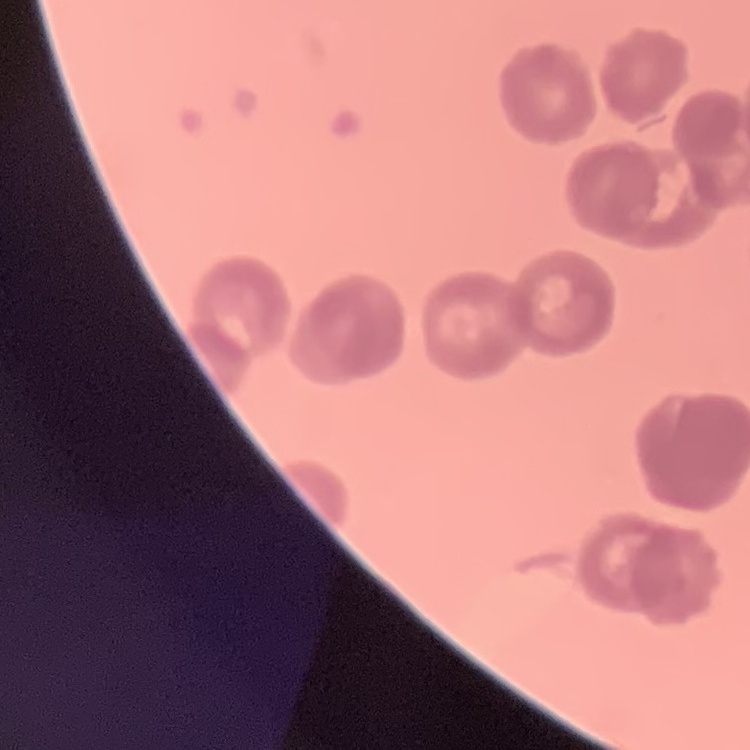

The erythrocytes show rouleaux formation. Field's or Giemsa stain. Thin blood film. One tile cut from a larger photomicrograph.